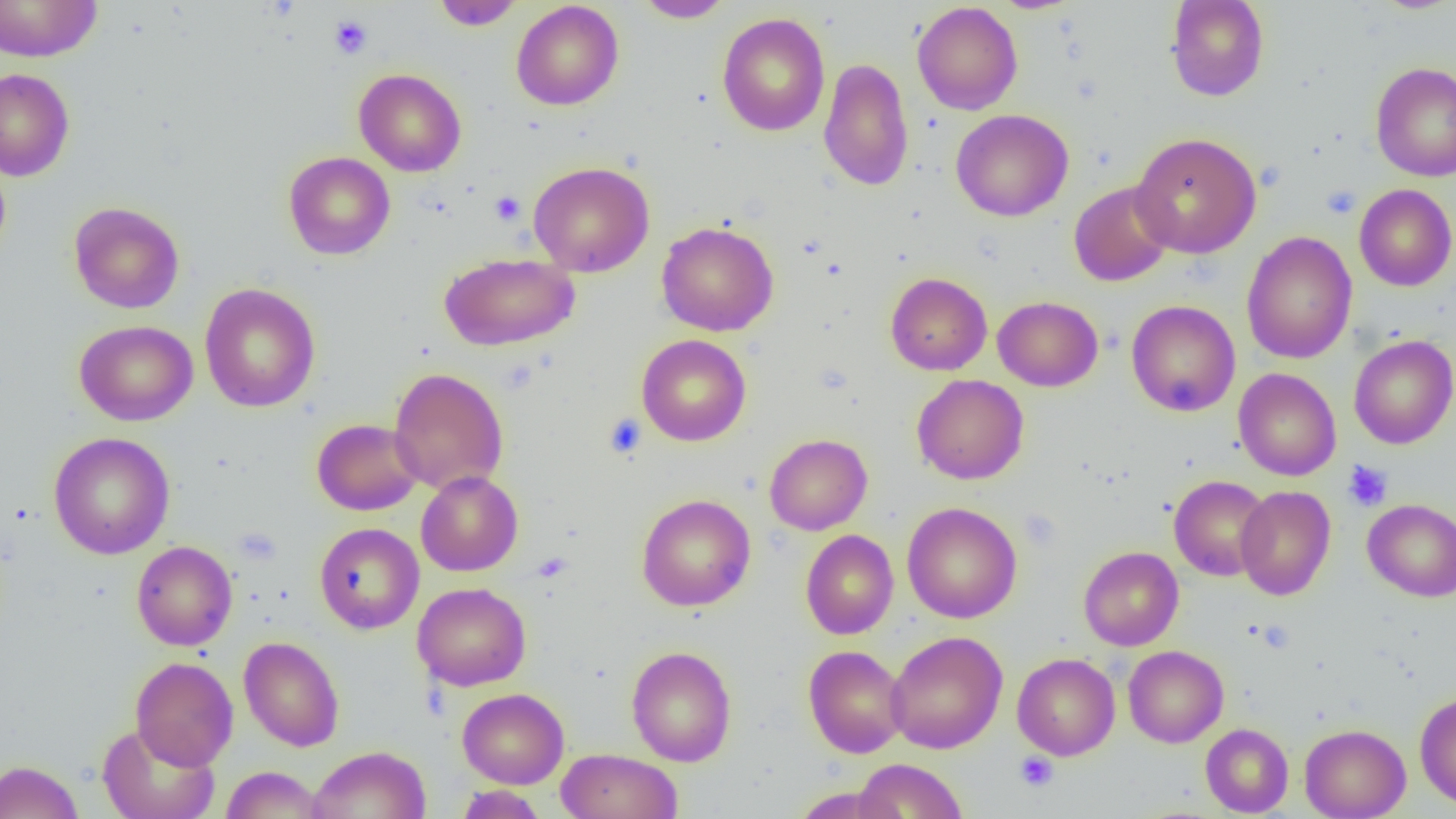
Summary:
  - Coordinate format: approximate bounding boxes as (x1, y1, x2, y2) in pixels
  - Uninfected red blood cell locations: (0, 0, 102, 62), (432, 0, 523, 30), (1165, 0, 1270, 101), (1375, 0, 1455, 14), (511, 1, 624, 110), (633, 1, 734, 22), (912, 2, 1023, 115), (717, 13, 830, 136), (818, 58, 914, 192), (1370, 61, 1456, 182), (0, 68, 75, 181), (353, 68, 467, 176), (951, 109, 1073, 222), (1130, 132, 1262, 258), (284, 151, 395, 260), (0, 155, 11, 267), (528, 161, 654, 277), (1069, 181, 1175, 287), (1354, 184, 1456, 291), (68, 201, 184, 314), (656, 221, 779, 337), (1242, 232, 1357, 364), (439, 252, 580, 351), (885, 272, 992, 375), (199, 283, 321, 412), (993, 296, 1103, 391), (1125, 299, 1241, 417), (74, 320, 198, 426), (637, 334, 751, 446), (1349, 335, 1456, 449), (388, 367, 509, 495), (1234, 368, 1341, 481), (912, 374, 1029, 485), (311, 418, 424, 516), (48, 432, 175, 559), (764, 433, 872, 535), (416, 470, 523, 576), (1169, 475, 1272, 581), (1235, 485, 1335, 601), (636, 493, 755, 612), (1362, 499, 1456, 602), (902, 501, 1022, 623), (314, 523, 424, 634), (800, 530, 898, 639), (131, 540, 237, 650), (1078, 546, 1184, 651), (412, 582, 531, 691), (885, 631, 1008, 753), (239, 636, 344, 751), (803, 645, 908, 758), (1123, 645, 1229, 747), (626, 646, 737, 766), (1012, 653, 1120, 760), (130, 656, 239, 769), (457, 688, 569, 788), (1414, 692, 1456, 809), (96, 723, 219, 819), (1200, 723, 1293, 816), (1299, 724, 1410, 819), (308, 745, 432, 819), (556, 748, 683, 819), (852, 758, 968, 819), (0, 760, 84, 819), (221, 766, 326, 818), (456, 785, 547, 819), (792, 786, 902, 819)
  - Platelet locations: (329, 15, 373, 59), (1321, 185, 1361, 218), (490, 191, 525, 225), (604, 414, 647, 459), (1343, 460, 1393, 511), (532, 552, 573, 583), (1256, 620, 1294, 653), (1015, 751, 1059, 792)
  - Slide-level diagnosis: negative for blood parasites
  - Modality: light microscopy
  - Preparation: thin blood film
  - Field of view: single
  - Magnification: 1000x
  - Image size: 1456×819 pixels